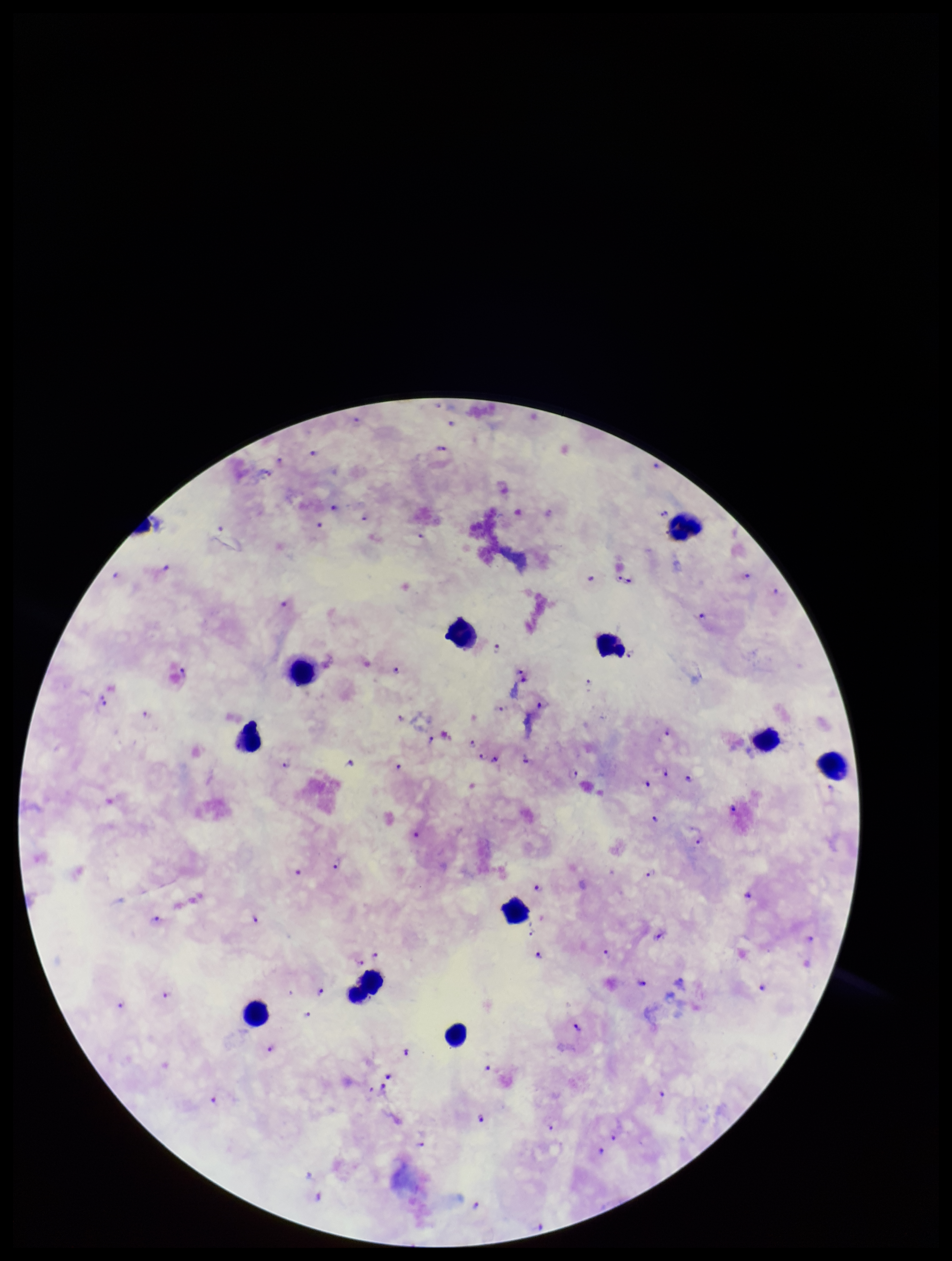

Species reported for this patient: Plasmodium falciparum. One field from this slide. Patient malaria status: positive. Plasmodium parasites: detected. Image is 952×1261 pixels. Parasite count: 80. Leukocyte count: 11. Stained with Giemsa. Smartphone photograph taken through the eyepiece of a microscope. Preparation: thick.